Give the position of every malaria parasite.
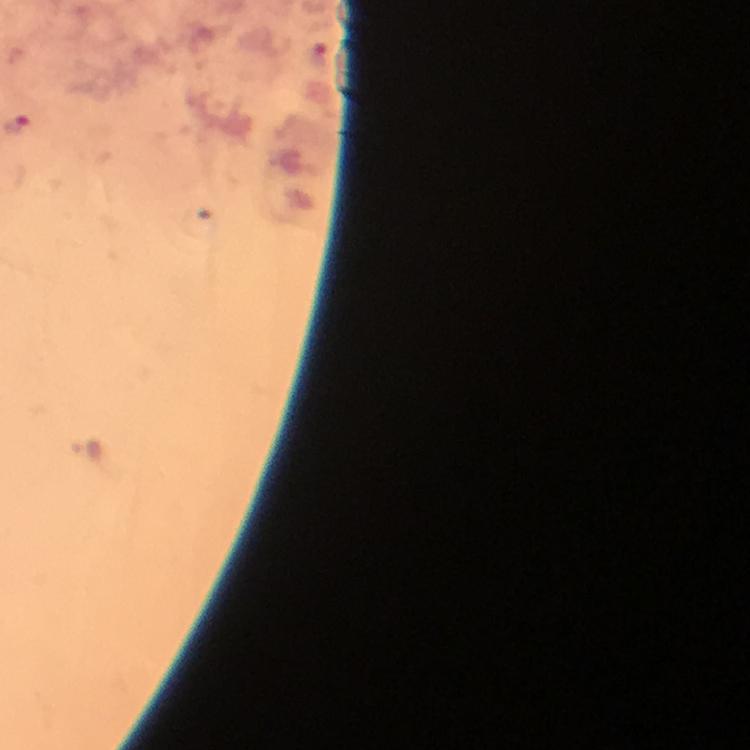
Approximate centers as [x, y] in pixels.
Malaria parasites: [19, 123].

stain = Giemsa
context = from a malaria diagnostic workup
magnification = 100x
cropped from = a single field of view
capture = smartphone camera through the microscope
preparation = thick smear
image size = 750×750 pixels
immersion oil = used